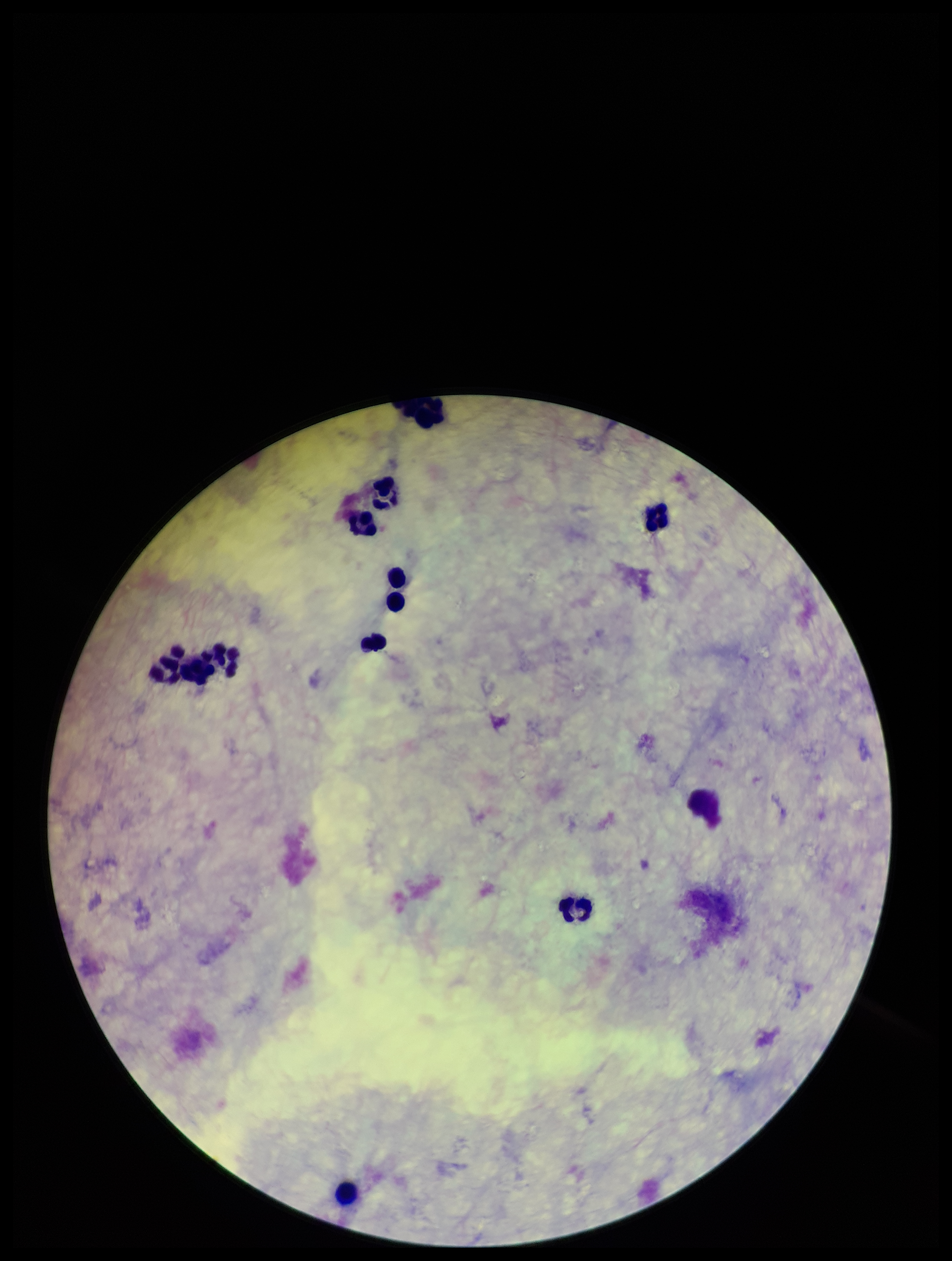

Single field of view. Photographed through the microscope eyepiece with a smartphone camera. Plasmodium parasites: none detected. Image is 952×1261 pixels. Parasite count: 0. Patient malaria status: negative. Preparation: thick smear. Leukocyte count: 11. Giemsa stain.